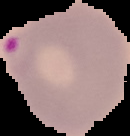
Summary:
  - Image size: 130×136 pixels
  - Preparation: thin blood smear
  - Image type: cell region segmented out of the field of view; surrounding area masked to black
  - Result: malaria parasites identified